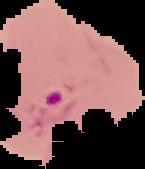

Summary:
  - Image type: segmented cell region with the area outside set to black
  - Malaria status: parasitized
  - Image size: 145×169 pixels
  - Preparation: thin blood film